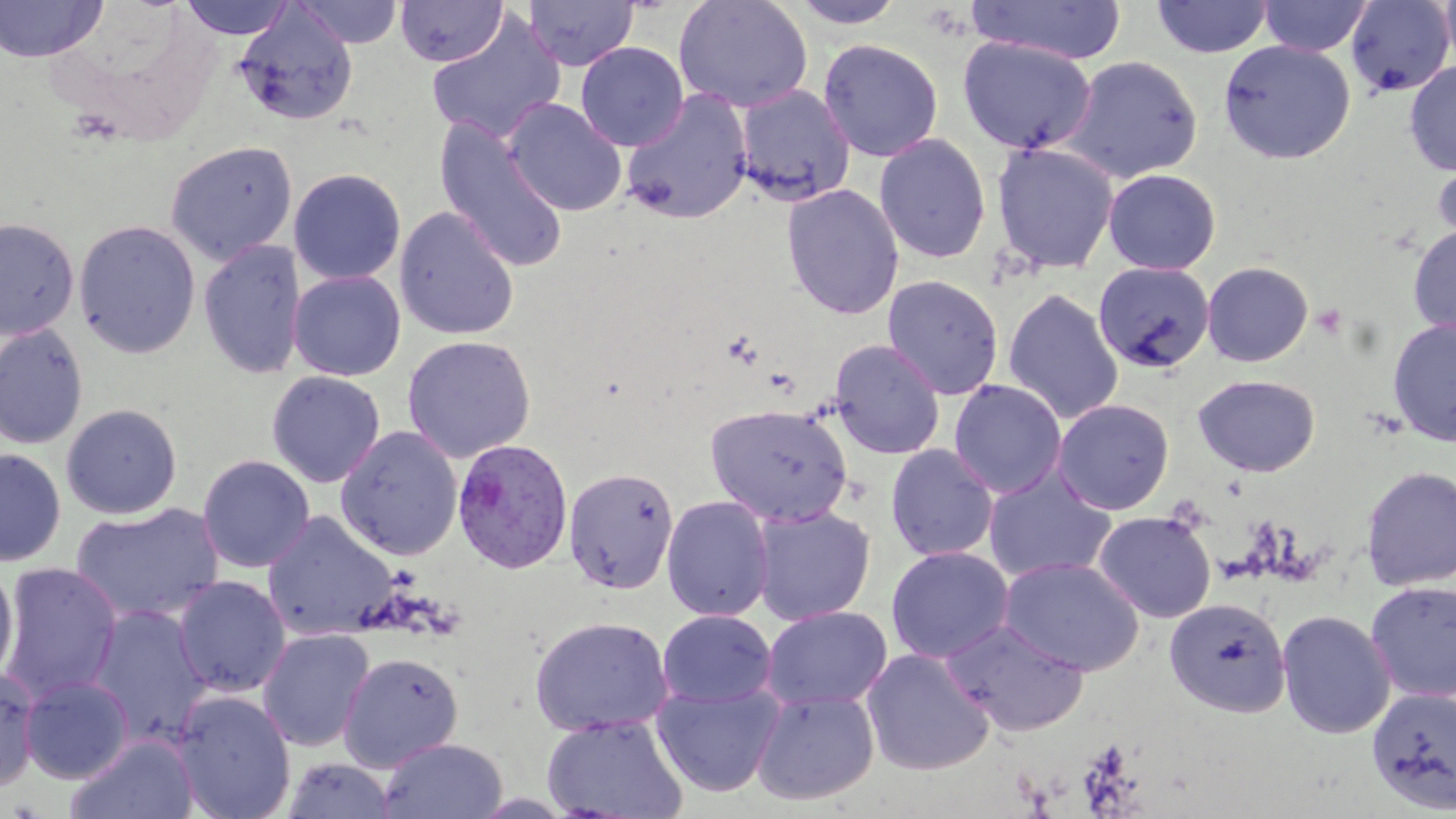

Approximate bounding boxes as [x1, y1, x2, y2] in pixels. Platelet locations: [1311, 303, 1348, 340]. Plasmodium vivax-infected red blood cell locations: [452, 438, 575, 574]. Uninfected red blood cell locations: [0, 0, 107, 62], [179, 0, 296, 40], [293, 0, 403, 48], [395, 0, 507, 66], [673, 0, 813, 113], [968, 0, 1126, 65], [1151, 0, 1273, 58], [1258, 0, 1372, 56], [1439, 0, 1456, 73], [522, 1, 638, 71], [789, 1, 906, 29], [1344, 1, 1455, 98], [234, 5, 358, 126], [426, 12, 565, 144], [957, 36, 1098, 155], [817, 39, 943, 162], [1218, 39, 1356, 164], [575, 41, 689, 151], [1062, 55, 1204, 183], [1404, 60, 1456, 176], [734, 84, 856, 206], [620, 88, 754, 224], [504, 98, 627, 216], [433, 116, 570, 274], [873, 133, 992, 264], [165, 141, 297, 265], [991, 141, 1120, 275], [1431, 151, 1456, 253], [1101, 167, 1222, 275], [288, 168, 406, 285], [781, 183, 905, 320], [394, 206, 520, 340], [1, 217, 79, 339], [74, 220, 201, 358], [1407, 223, 1456, 338], [199, 240, 306, 380], [1093, 260, 1215, 375], [1201, 260, 1314, 367], [288, 270, 406, 381], [882, 275, 1004, 400], [1003, 288, 1124, 425], [1386, 315, 1456, 447], [0, 323, 88, 450], [402, 335, 536, 464], [829, 339, 945, 459], [266, 371, 385, 487], [1192, 374, 1321, 477], [949, 379, 1067, 498], [1052, 398, 1175, 515], [704, 403, 853, 526], [61, 404, 182, 519], [335, 425, 462, 561], [885, 444, 999, 562], [0, 448, 66, 566], [197, 454, 315, 573], [1360, 464, 1456, 591], [982, 465, 1118, 583], [563, 467, 680, 594], [662, 495, 774, 621], [71, 503, 223, 624], [751, 505, 875, 625], [1092, 510, 1217, 623], [261, 511, 399, 641], [885, 546, 1014, 663], [999, 555, 1144, 676], [1, 562, 122, 703], [0, 563, 18, 687], [173, 576, 290, 697], [1364, 579, 1456, 702], [1164, 596, 1292, 718], [87, 605, 212, 746], [760, 606, 892, 712], [1276, 608, 1396, 740], [656, 609, 778, 708], [529, 615, 674, 736], [943, 619, 1090, 736], [257, 628, 375, 753], [861, 648, 995, 776], [338, 651, 464, 772], [0, 666, 41, 791], [20, 675, 134, 784], [653, 681, 784, 797], [1366, 684, 1456, 815], [750, 689, 879, 806], [173, 690, 296, 819], [542, 714, 688, 818], [67, 734, 199, 819], [378, 738, 508, 818], [283, 757, 396, 818]. Slide-level diagnosis: Plasmodium vivax. One field of a larger specimen. Optical microscopy. Captured at 1000x magnification. Image is 1456×819 pixels. May-Grünwald-Giemsa stain. Thin blood smear.